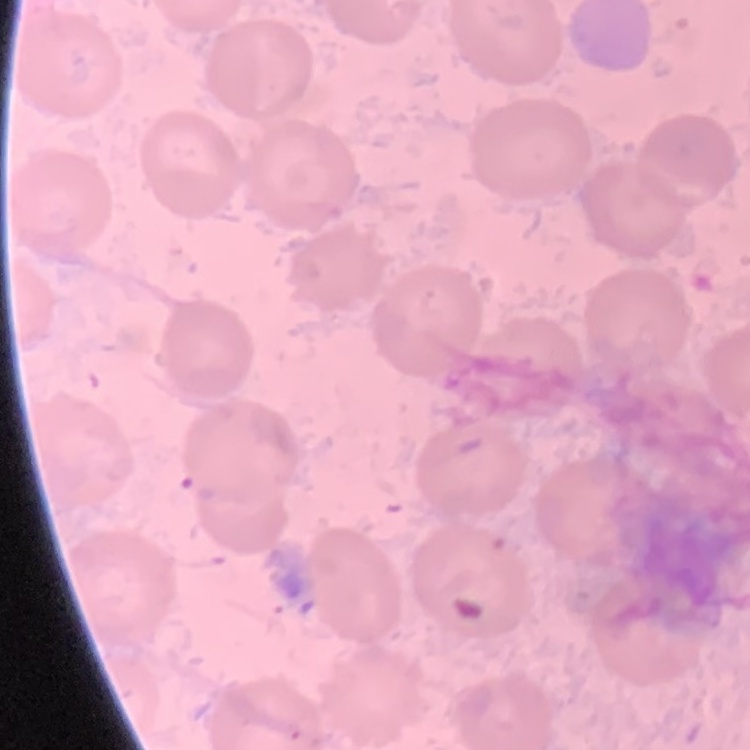 The erythrocytes show no rouleaux formation. Stained with either Field's or Giemsa. Thin peripheral smear. One tile cut from a larger photomicrograph.